Identify the parasite.
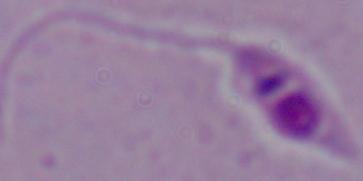
This is Leishmania.

Summary:
  - Modality: micrograph
  - Magnification: 1000x